Report the malaria status of this cell.
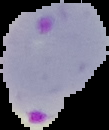
Parasitized.

preparation: thin blood film
image_size: 109×130 pixels
image_type: cell region segmented out of the field of view; surrounding area masked to black